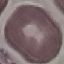

Result: no malaria parasites detected. Acquired by smartphone through the microscope eyepiece. Giemsa-stained preparation. Thin smear of blood. Cell patch, automatically extracted from a larger field of view and resized to 64 × 64 pixels.